Comment on the morphology of the erythrocytes.
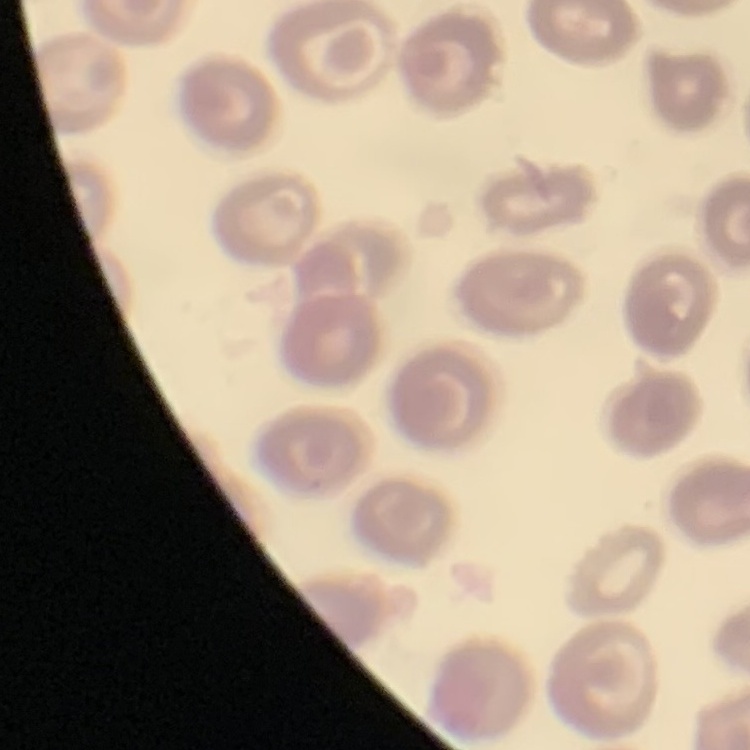

No rouleaux formation.

One tile cut from a larger photomicrograph. Thin blood smear. Field's or Giemsa stain.